Identify the blood parasite species.
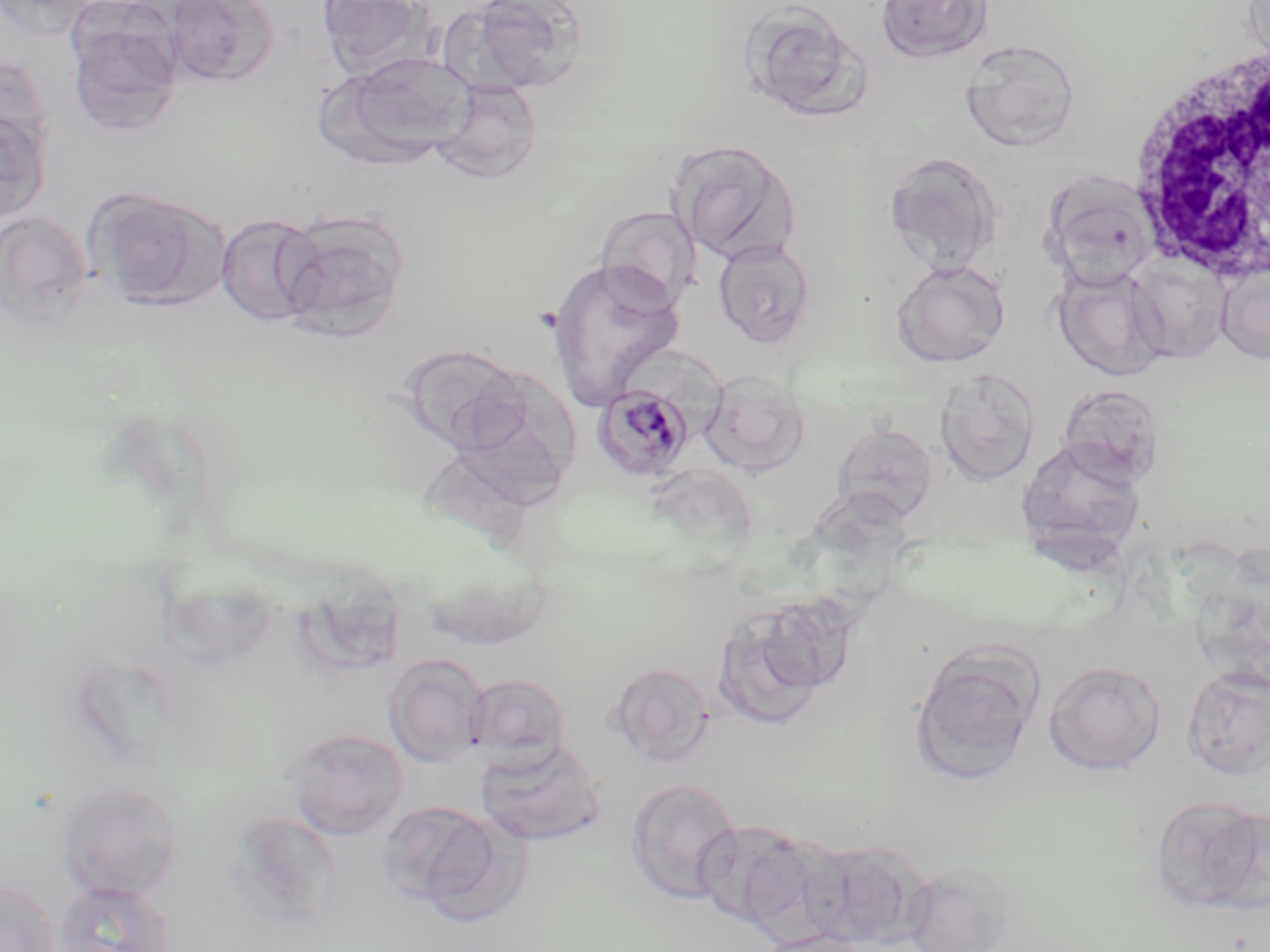
Plasmodium malariae.

{
  "stain": "May-Grünwald-Giemsa",
  "magnification": "1000x",
  "preparation": "thin blood smear",
  "field_of_view": "single",
  "white_blood_cell_locations": "approximate bounding boxes as [x1, y1, x2, y2] in pixels: [1124, 38, 1267, 287]",
  "plasmodium_malariae_infected_red_blood_cell_locations": "approximate bounding boxes as [x1, y1, x2, y2] in pixels: [591, 382, 695, 481]",
  "uninfected_red_blood_cell_locations": "approximate bounding boxes as [x1, y1, x2, y2] in pixels: [316, 0, 433, 79], [456, 0, 588, 95], [875, 0, 994, 64], [163, 1, 278, 88], [736, 1, 870, 121], [65, 5, 185, 137], [960, 38, 1080, 151], [324, 51, 474, 166], [0, 54, 55, 172], [433, 79, 544, 183], [0, 109, 51, 223], [667, 140, 801, 265], [883, 152, 1003, 276], [1043, 177, 1157, 290], [84, 187, 227, 309], [597, 206, 700, 311], [0, 209, 92, 331], [276, 209, 409, 340], [215, 214, 326, 328], [711, 236, 819, 348], [548, 257, 686, 408], [1129, 257, 1230, 364], [892, 259, 1010, 368], [1216, 263, 1270, 364], [1053, 266, 1169, 381], [396, 343, 529, 457], [448, 366, 580, 508], [935, 368, 1040, 487], [700, 369, 809, 474], [1057, 383, 1167, 485], [831, 421, 939, 524], [1017, 438, 1147, 556], [708, 596, 847, 729], [910, 646, 1043, 786], [384, 654, 487, 766], [1043, 659, 1167, 776], [608, 662, 715, 765], [1181, 664, 1270, 782], [465, 673, 572, 771], [284, 726, 409, 840], [475, 738, 608, 847], [624, 777, 742, 906], [56, 780, 184, 901], [1148, 793, 1269, 917], [377, 799, 505, 912], [225, 810, 345, 931], [692, 819, 814, 928], [797, 840, 923, 948], [900, 862, 1019, 952], [0, 879, 59, 952], [53, 880, 175, 952], [752, 928, 872, 952]",
  "modality": "optical microscopy",
  "image_size": "1270×952 pixels"
}